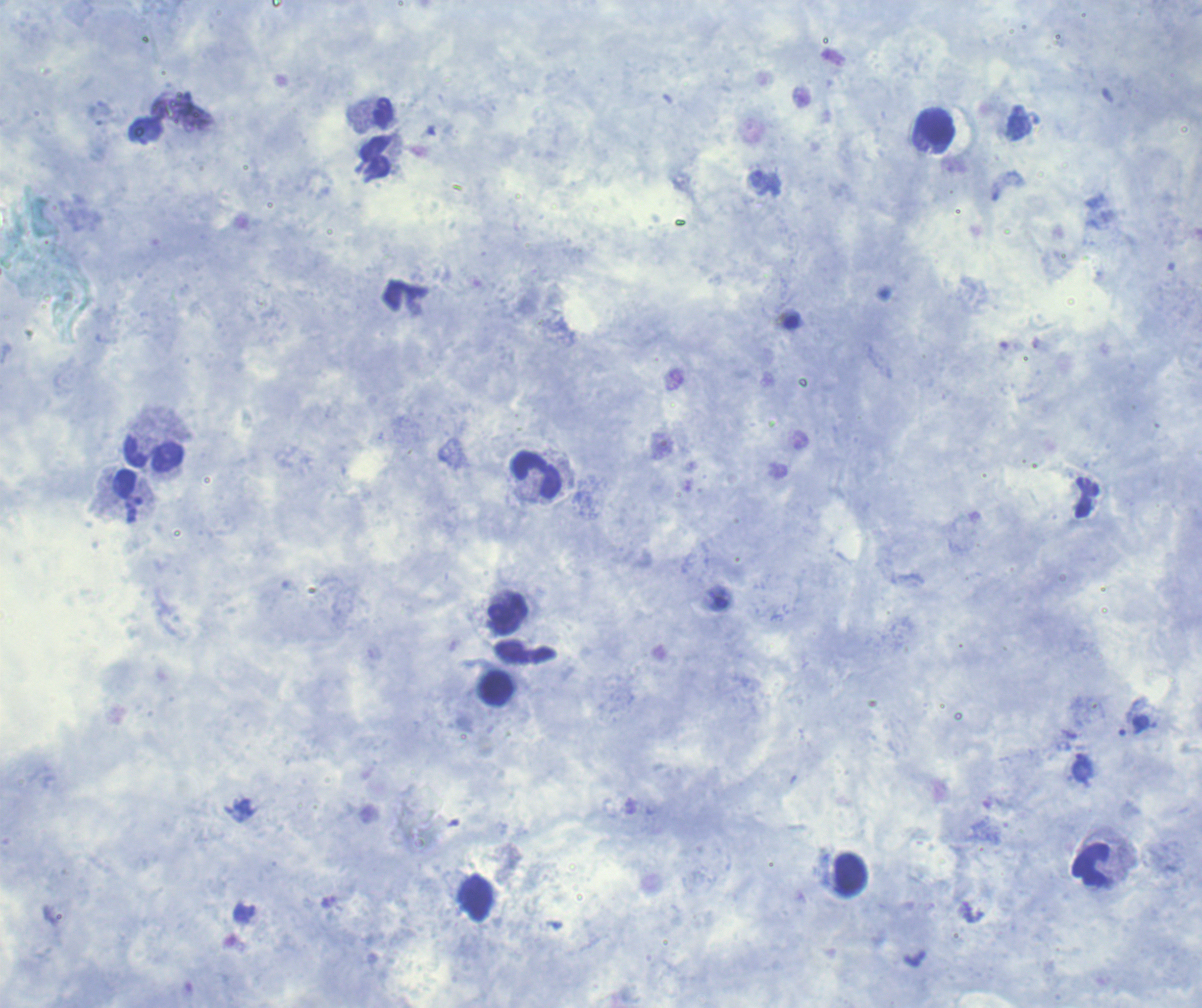

Approximate centers as [x, y] in pixels. Leukocyte locations: [384, 114], [936, 128], [375, 158], [154, 453], [538, 475], [508, 615], [497, 688], [1091, 866], [851, 875], [476, 898]. Trophozoite locations: [765, 183]. 100x magnification. Previously used in a real diagnosis. Coloration quality: good. Result: malaria parasites detected. Thick blood smear. Romanowsky-stained preparation. Background quality: good. One field from this slide. Image is 1202×1008 pixels.